Classify this cell by malaria status.
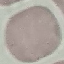
Uninfected.

preparation = thin blood smear
image type = cell patch, automatically extracted from a larger field of view and resized to 64 × 64 pixels
stain = Giemsa
capture = smartphone camera at the microscope eyepiece